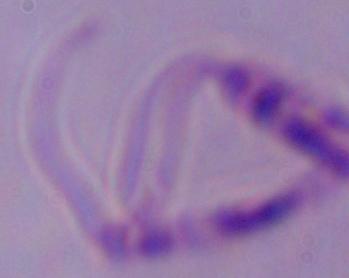

Summary:
  - Modality: photomicrograph
  - Identification: Leishmania
  - Magnification: 1000x